Assess the morphology of the erythrocytes.
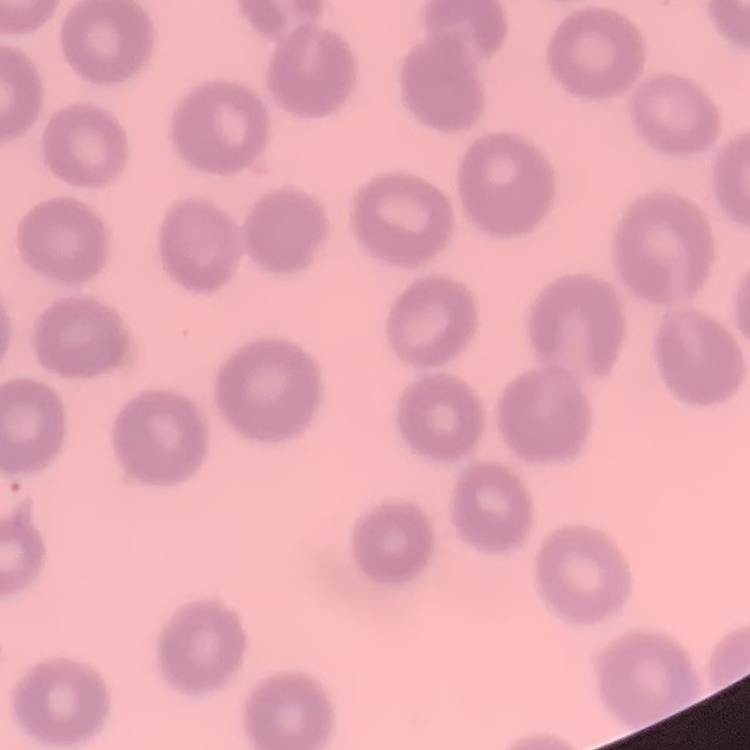

No rouleaux formation.

Thin blood film. One tile cut from a larger photomicrograph. Field's or Giemsa stain.